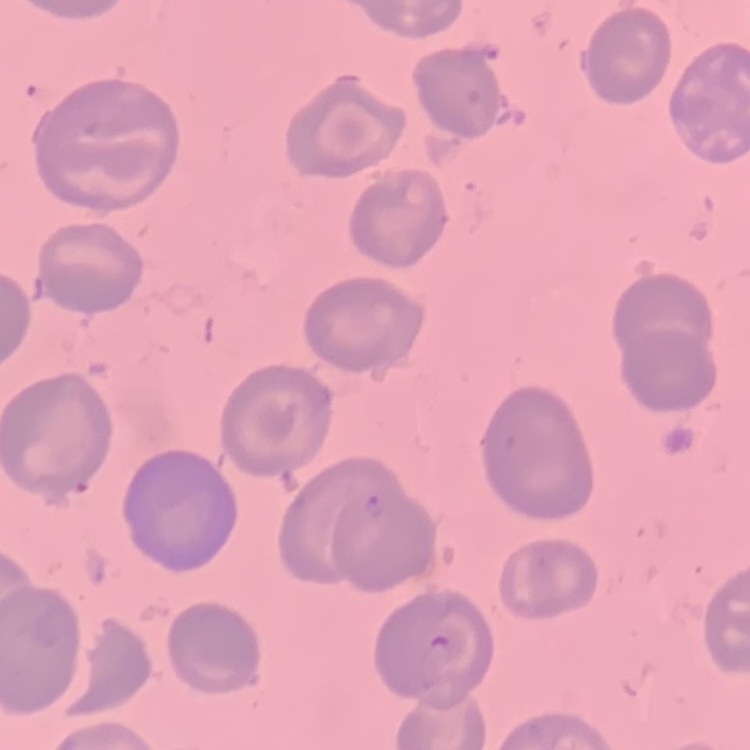
The red blood cells exhibit no rouleaux formation. Stained with either Field's or Giemsa. Square crop of a larger photomicrograph. Thin blood smear.